Assess the morphology of the red blood cells.
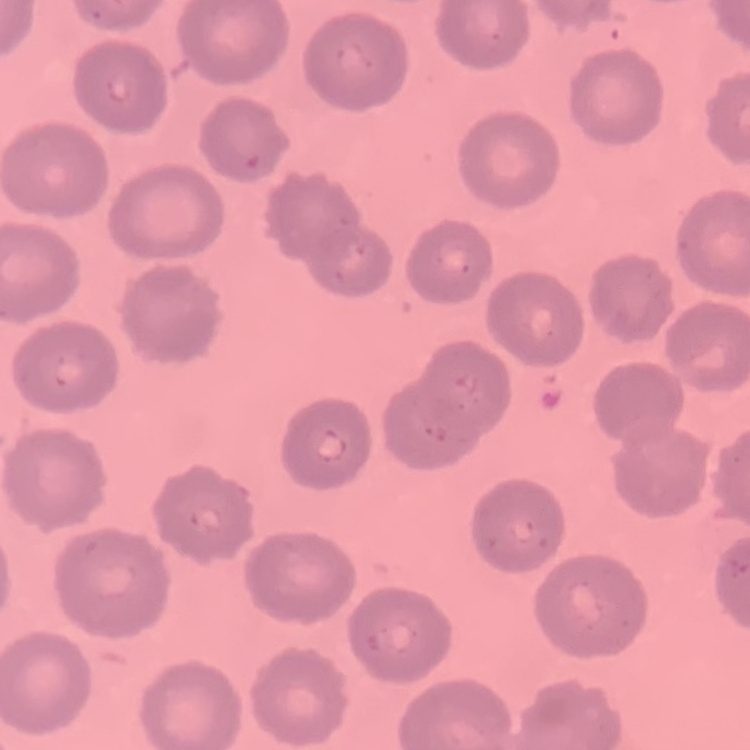
No rouleaux formation.

{
  "stain": "Field's or Giemsa",
  "image_type": "one tile cut from a larger photomicrograph",
  "preparation": "thin blood smear"
}